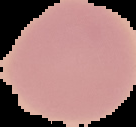

image type = cell region segmented out of the field of view; surrounding area masked to black
image size = 136×127 pixels
malaria status = uninfected
preparation = thin blood smear